Locate every blood parasite and identify its species.
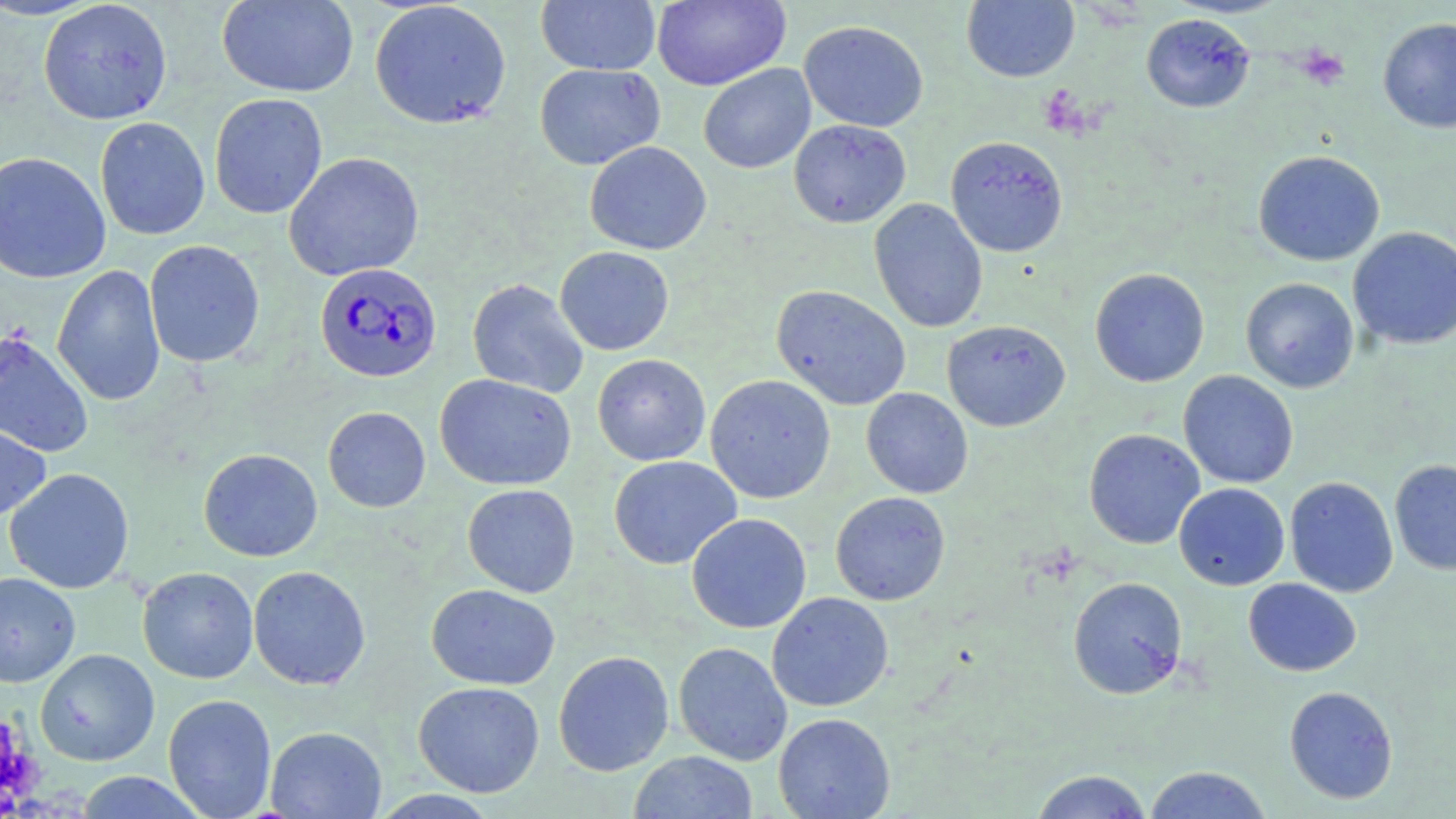

Approximate bounding boxes as [x1, y1, x2, y2] in pixels.
Plasmodium falciparum-infected red blood cells: [314, 262, 442, 384].
No Plasmodium ovale, Plasmodium malariae, Plasmodium vivax, Babesia divergens, or Trypanosoma brucei observed.

{
  "slide_level_diagnosis": "Plasmodium falciparum",
  "field_of_view": "one of a larger specimen",
  "image_size": "1456×819 pixels",
  "platelet_locations": "approximate bounding boxes as [x1, y1, x2, y2] in pixels: [1299, 46, 1349, 89], [0, 713, 42, 805]",
  "uninfected_red_blood_cell_locations": "approximate bounding boxes as [x1, y1, x2, y2] in pixels: [216, 0, 359, 97], [652, 0, 790, 90], [1166, 0, 1289, 18], [37, 1, 173, 125], [368, 1, 511, 130], [536, 1, 661, 75], [962, 1, 1079, 83], [1141, 13, 1255, 112], [1378, 17, 1456, 133], [799, 20, 929, 133], [534, 63, 665, 170], [698, 64, 816, 174], [209, 93, 328, 219], [95, 117, 210, 240], [788, 119, 911, 228], [946, 135, 1068, 257], [585, 141, 712, 256], [1253, 150, 1385, 267], [0, 151, 111, 284], [283, 152, 424, 281], [869, 198, 988, 334], [1347, 226, 1456, 350], [144, 240, 265, 367], [555, 246, 674, 356], [52, 264, 166, 407], [1089, 268, 1210, 387], [1241, 278, 1359, 393], [467, 279, 589, 398], [771, 285, 912, 411], [942, 319, 1071, 432], [0, 330, 94, 458], [592, 354, 711, 466], [1178, 370, 1298, 488], [435, 373, 577, 491], [705, 374, 836, 504], [861, 387, 973, 498], [323, 406, 431, 512], [0, 419, 52, 523], [1083, 428, 1204, 549], [198, 448, 323, 562], [609, 455, 741, 570], [1389, 460, 1456, 575], [3, 467, 135, 594], [1284, 477, 1398, 598], [1174, 483, 1290, 590], [462, 484, 580, 597], [830, 491, 950, 605], [686, 513, 812, 634], [248, 565, 371, 690], [137, 566, 258, 684], [0, 572, 82, 687], [1068, 576, 1188, 699], [1244, 578, 1361, 676], [426, 583, 561, 690], [767, 592, 894, 712], [673, 642, 793, 765], [35, 648, 160, 767], [553, 650, 674, 776], [413, 681, 545, 797], [1284, 685, 1398, 804], [163, 693, 277, 818], [773, 712, 895, 818], [265, 726, 387, 818], [629, 751, 758, 819], [1143, 765, 1273, 818], [1030, 769, 1154, 818], [73, 771, 208, 818]",
  "magnification": "1000x",
  "modality": "light microscopy",
  "stain": "May-Grünwald-Giemsa",
  "preparation": "thin blood film"
}